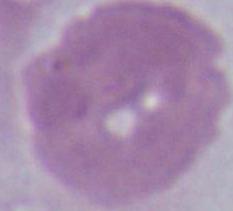
identification = erythrocyte
magnification = 1000x
modality = micrograph